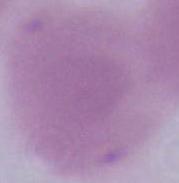

Summary:
  - Modality: micrograph
  - Magnification: 1000x
  - Identification: erythrocyte